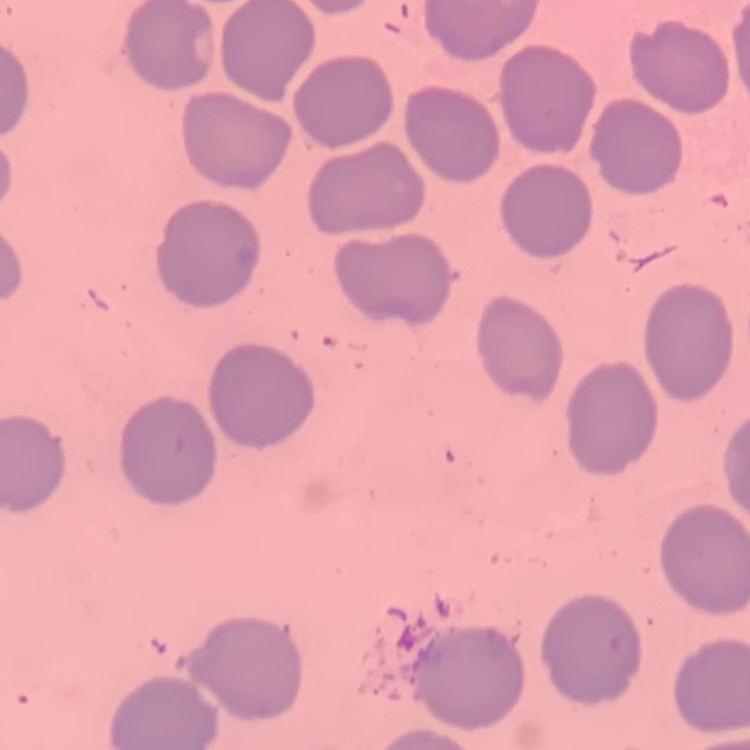

The red blood cells show no rouleaux formation. One tile cut from a larger photomicrograph. Thin blood film. Stained with either Field's or Giemsa.